Classify this cell by malaria status.
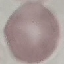
It is uninfected.

stain = Giemsa
preparation = thin blood film
image type = cell patch, automatically extracted from a larger field of view and resized to 64 × 64 pixels
capture = smartphone through the microscope eyepiece